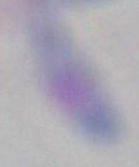
Summary:
  - Magnification: 1000x
  - Modality: photomicrograph
  - Identification: Toxoplasma gondii